Classify this cell by malaria status.
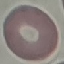

It is uninfected.

Thin blood film. Acquired by smartphone through the microscope eyepiece. Giemsa stain. Cell patch, automatically extracted from a larger field of view and resized to 64 × 64 pixels.